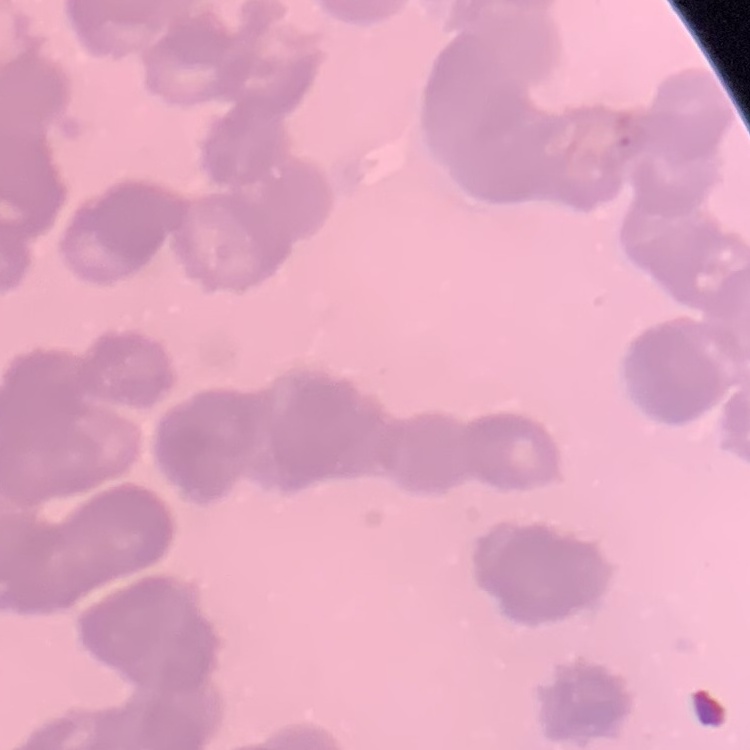

red_blood_cell_morphology: rouleaux formation
image_type: square crop of a larger photomicrograph
preparation: thin peripheral smear
stain: Field's or Giemsa